Point out each Plasmodium parasite and each leukocyte.
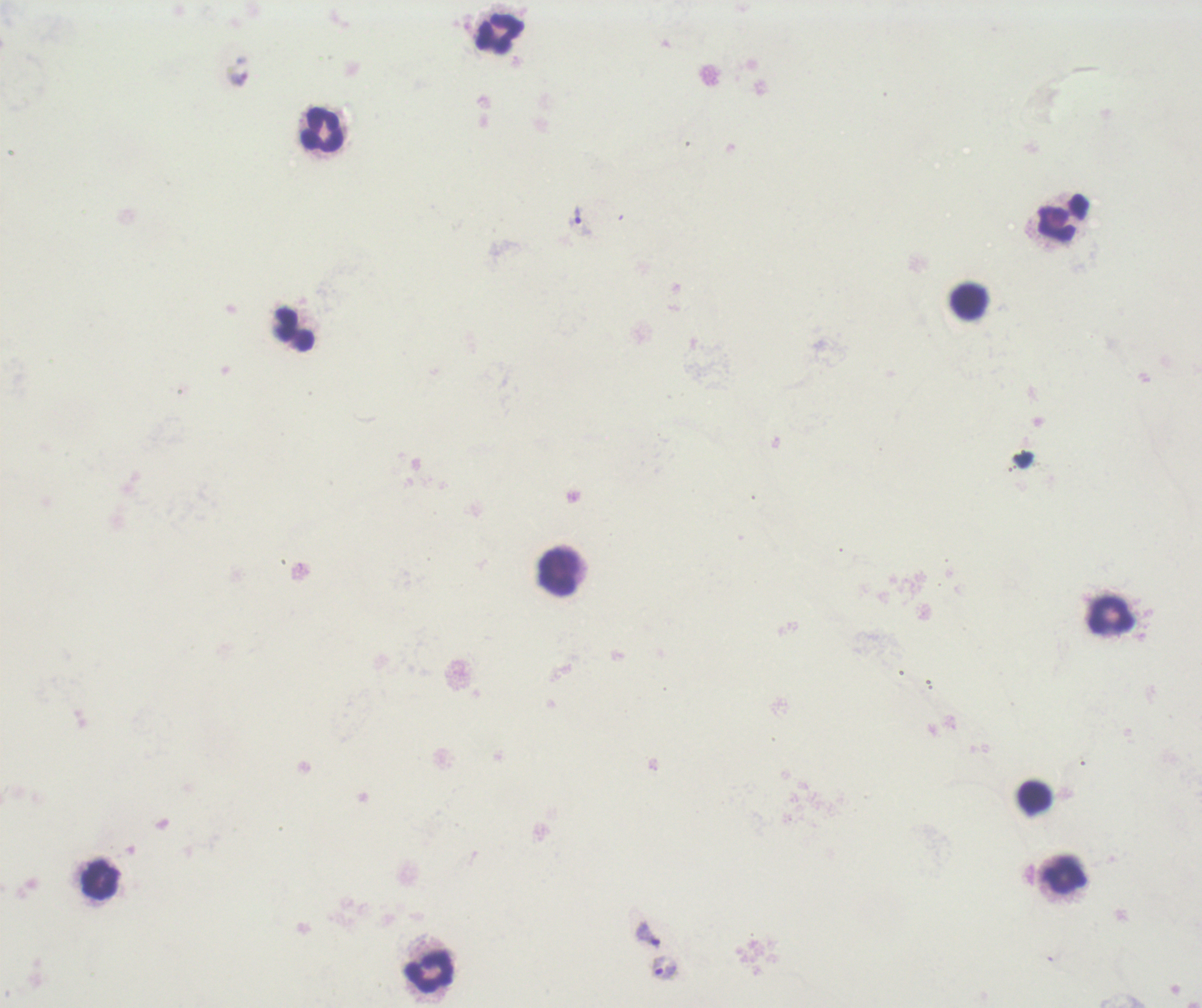
Approximate centers as (x, y) in pixels.
Trophozoites: (237, 71), (577, 215), (648, 934), (665, 969).
No schizont or gametocyte forms observed.
Leukocytes: (500, 35), (322, 129), (1063, 218), (968, 301), (294, 330), (559, 573), (1110, 616), (1035, 797), (1065, 875), (100, 880), (430, 971).

image_size: 1202×1008 pixels
coloration_quality: bad
background_quality: unsatisfactory
context: previously used in an actual diagnosis
magnification: 100x
field_of_view: single
preparation: thick smear of blood
stain: Romanowsky